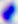

Micrograph. Toxoplasma gondii is shown. 400x magnification.